Look for Plasmodium parasites.
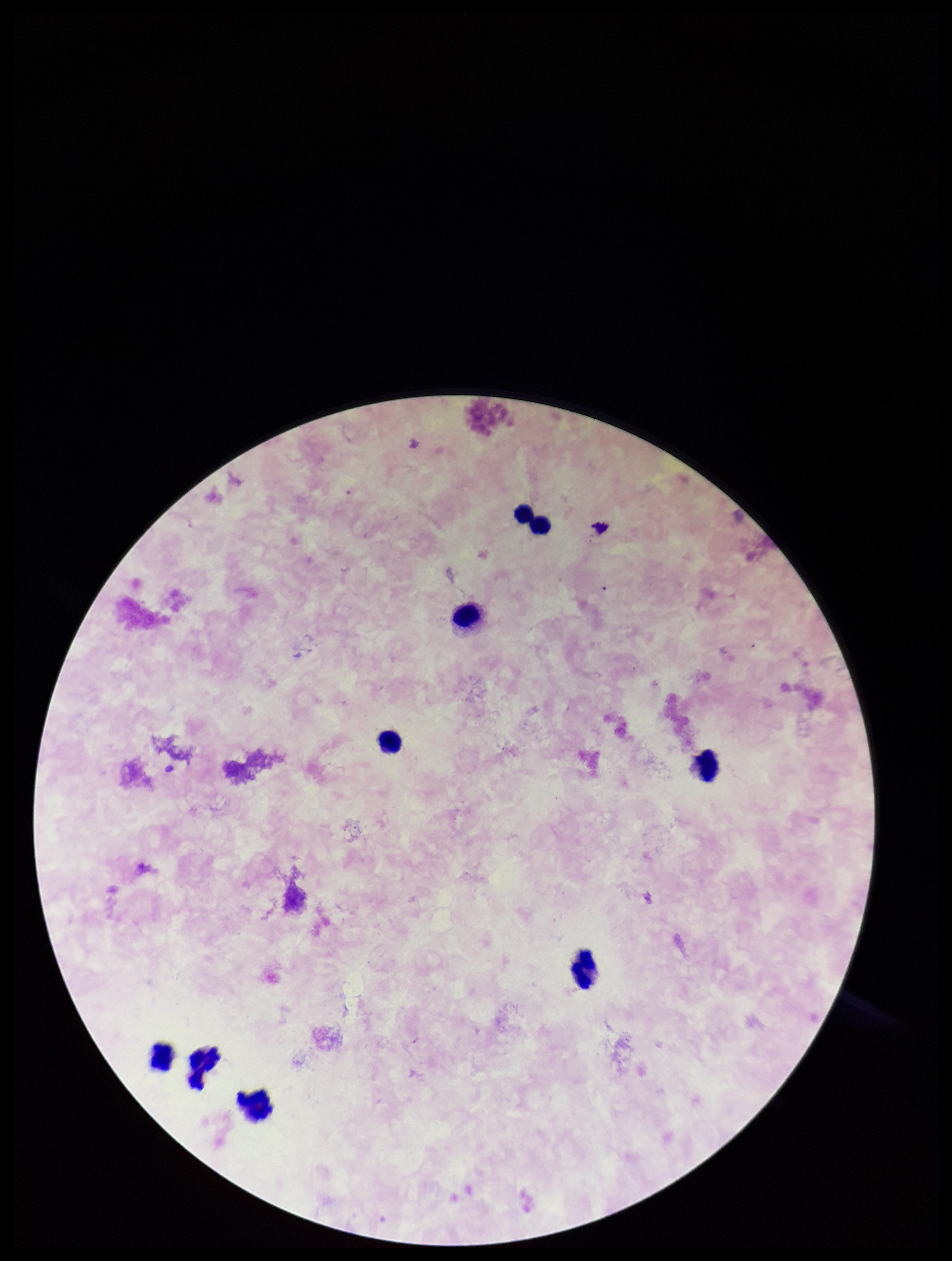
None detected.

Summary:
  - Parasite count: 0
  - Image size: 952×1261 pixels
  - Leukocyte count: 9
  - Capture: smartphone photograph through the microscope eyepiece
  - Preparation: thick
  - Stain: Giemsa
  - Field of view: one from this slide
  - Patient malaria status: negative